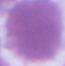

A red blood cell is shown. Captured at 1000x magnification. Photomicrograph.